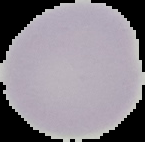 Malaria status: uninfected. From a thin blood film. Image is 145×142 pixels. The area outside the segmented cell region is set to black.